State the blood parasite species.
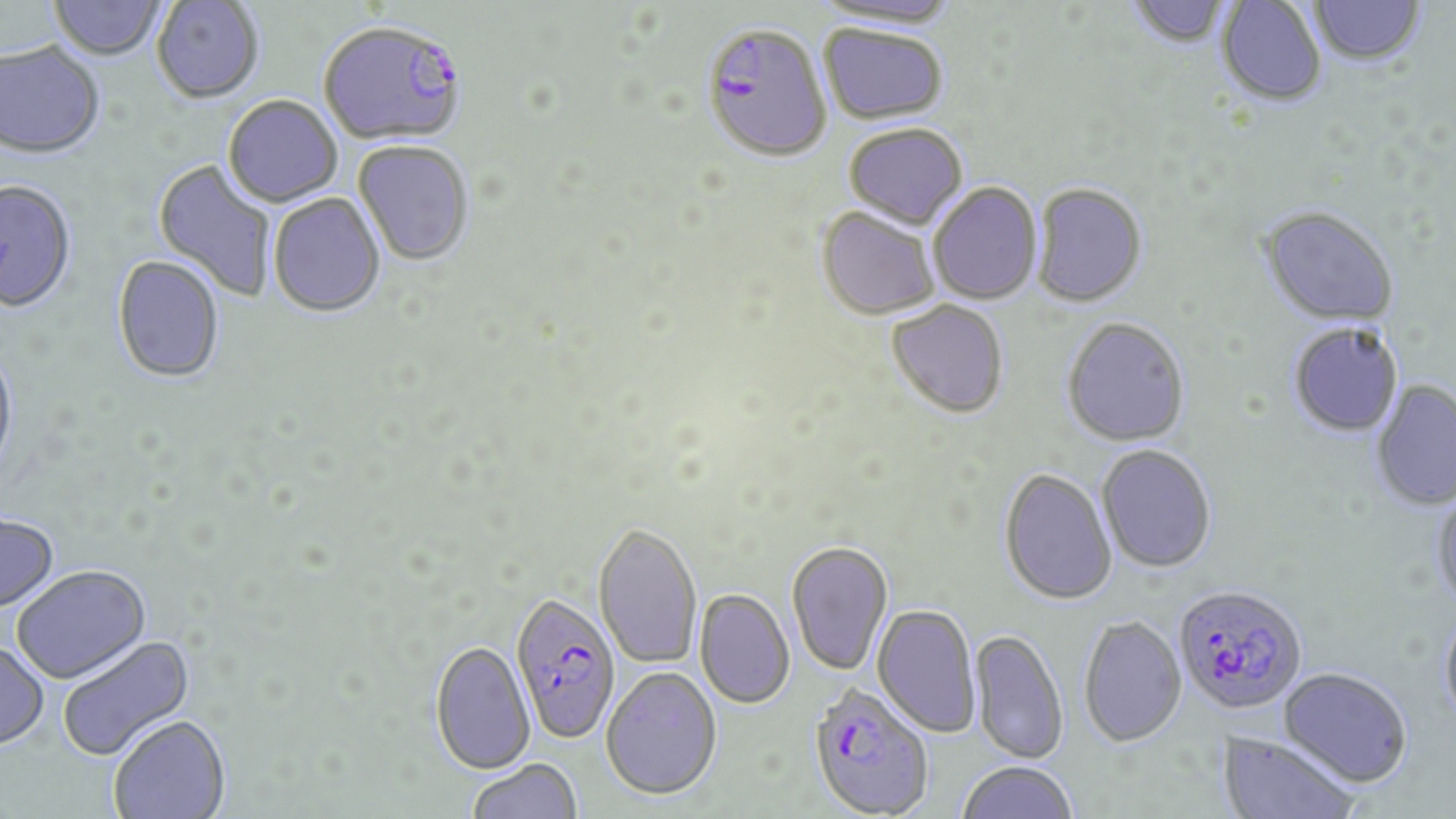

Plasmodium falciparum.

modality = optical microscopy
Plasmodium falciparum-infected red blood cell locations = approximate bounding boxes as [x1, y1, x2, y2] in pixels: [317, 18, 467, 145], [701, 21, 832, 161], [1173, 583, 1308, 715], [509, 593, 621, 743], [807, 682, 934, 818]
uninfected red blood cell locations = approximate bounding boxes as [x1, y1, x2, y2] in pixels: [50, 0, 167, 60], [814, 0, 962, 28], [1126, 0, 1233, 48], [1217, 0, 1327, 105], [152, 1, 264, 103], [1309, 1, 1424, 65], [819, 23, 949, 125], [0, 41, 104, 157], [223, 94, 342, 206], [844, 122, 968, 229], [353, 140, 474, 266], [153, 159, 277, 303], [1, 179, 77, 312], [927, 181, 1043, 305], [1032, 182, 1147, 307], [268, 193, 386, 318], [1259, 205, 1399, 327], [815, 206, 941, 321], [113, 256, 224, 383], [887, 300, 1009, 418], [1062, 317, 1190, 446], [1288, 322, 1404, 437], [0, 344, 18, 481], [1371, 379, 1456, 510], [1097, 444, 1217, 573], [999, 467, 1117, 604], [1431, 488, 1456, 609], [0, 513, 60, 614], [593, 520, 702, 669], [786, 540, 893, 676], [12, 564, 151, 684], [695, 588, 795, 709], [873, 603, 981, 738], [1439, 607, 1456, 728], [1078, 614, 1187, 746], [970, 628, 1069, 764], [57, 634, 194, 762], [430, 639, 536, 774], [0, 641, 49, 750], [601, 665, 722, 800], [1279, 666, 1413, 788], [108, 715, 231, 819], [1219, 731, 1359, 819], [467, 758, 582, 819], [957, 760, 1078, 819]
field of view = single
image size = 1456×819 pixels
preparation = thin blood film
stain = May-Grünwald-Giemsa
magnification = 1000x